Assess this cell for malaria.
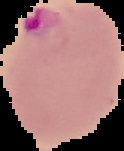
Parasitized.

Summary:
  - Image size: 124×151 pixels
  - Image type: segmented cell region with the area outside set to black
  - Preparation: thin blood smear